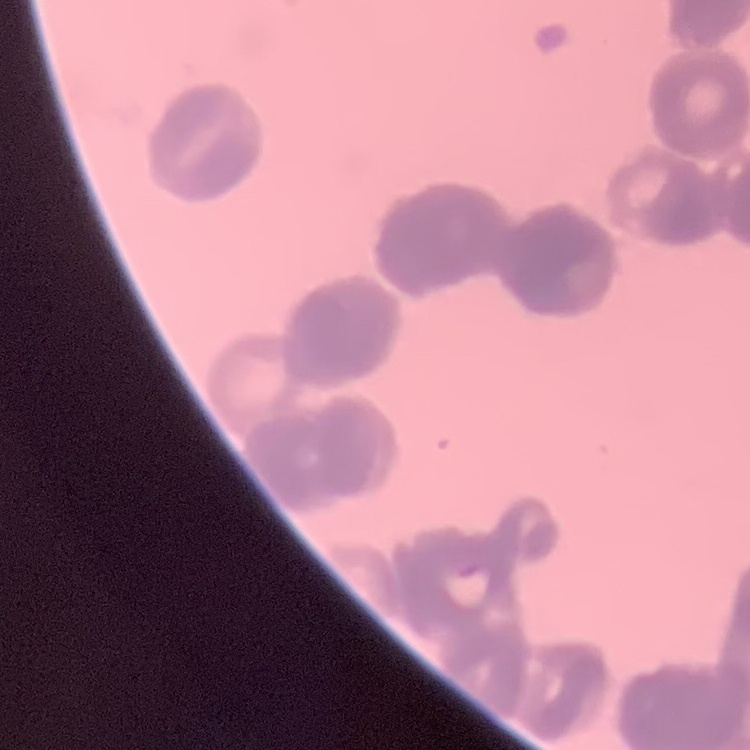

{
  "erythrocyte_morphology": "rouleaux formation",
  "stain": "Field's or Giemsa",
  "image_type": "one tile cut from a larger photomicrograph",
  "preparation": "thin blood smear"
}